Locate and identify every blood parasite.
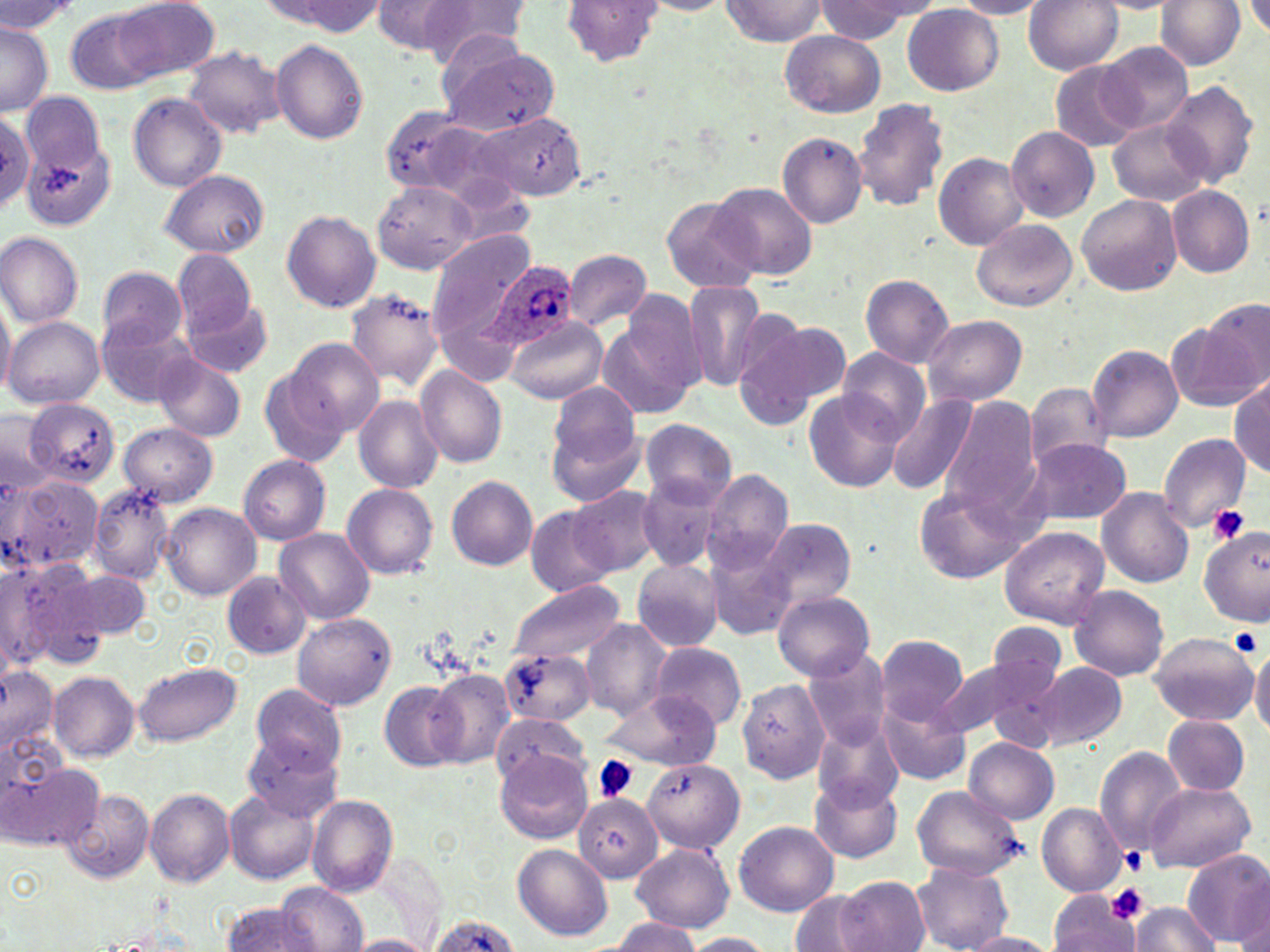

Approximate bounding boxes as (x1, y1, x2, y2) in pixels.
Plasmodium ovale-infected red blood cells: (476, 259, 580, 351).
No Plasmodium falciparum, Plasmodium malariae, Plasmodium vivax, Babesia divergens, or Trypanosoma brucei observed.

Uninfected red blood cell locations: (114, 0, 220, 82), (370, 0, 472, 56), (561, 0, 663, 67), (720, 0, 827, 47), (951, 0, 1052, 18), (1025, 0, 1122, 75), (1156, 0, 1243, 69), (1, 1, 80, 36), (266, 1, 385, 36), (425, 1, 533, 71), (641, 1, 733, 15), (817, 1, 926, 41), (1089, 1, 1179, 14), (1244, 2, 1270, 40), (903, 5, 1003, 95), (65, 6, 163, 93), (0, 24, 52, 114), (780, 31, 885, 117), (269, 39, 369, 144), (1099, 41, 1194, 134), (184, 46, 287, 138), (439, 47, 559, 136), (1048, 60, 1144, 152), (1161, 80, 1261, 186), (21, 91, 106, 175), (128, 93, 227, 192), (852, 98, 951, 212), (377, 107, 483, 196), (1, 110, 37, 213), (469, 112, 588, 200), (1108, 118, 1209, 205), (1006, 125, 1099, 222), (22, 133, 117, 232), (777, 133, 867, 228), (933, 152, 1028, 250), (159, 169, 269, 257), (373, 182, 477, 275), (709, 182, 817, 280), (1167, 185, 1256, 277), (1077, 194, 1182, 297), (661, 196, 762, 294), (281, 211, 380, 311), (973, 219, 1078, 311), (427, 228, 537, 361), (0, 231, 85, 327), (565, 249, 651, 329), (171, 250, 261, 338), (97, 266, 187, 350), (861, 274, 955, 367), (681, 281, 768, 391), (0, 284, 15, 401), (346, 287, 443, 390), (624, 288, 755, 403), (182, 295, 273, 376), (1201, 299, 1269, 393), (599, 306, 702, 420), (96, 311, 196, 407), (730, 311, 842, 426), (4, 314, 106, 410), (923, 315, 1027, 405), (504, 316, 607, 402), (1168, 323, 1260, 413), (284, 340, 384, 439), (1087, 344, 1184, 441), (835, 348, 929, 444), (152, 351, 247, 443), (259, 365, 352, 470), (416, 365, 507, 468), (1230, 375, 1270, 475), (1024, 383, 1114, 467), (547, 384, 642, 485), (804, 392, 904, 492), (888, 393, 981, 497), (355, 395, 442, 494), (938, 396, 1040, 516), (17, 399, 122, 488), (1, 406, 53, 486), (639, 418, 736, 507), (120, 422, 217, 506), (1157, 433, 1251, 531), (1020, 437, 1134, 527), (238, 454, 330, 545), (703, 469, 793, 571), (636, 473, 725, 573), (8, 475, 105, 574), (447, 476, 537, 570), (89, 483, 176, 583), (344, 483, 438, 578), (914, 484, 1030, 582), (568, 487, 665, 576), (1096, 488, 1194, 588), (162, 503, 262, 599), (525, 506, 616, 595), (756, 517, 856, 611), (999, 526, 1109, 628), (1199, 526, 1268, 626), (276, 528, 374, 623), (704, 541, 799, 641), (631, 558, 723, 653), (0, 560, 60, 671), (24, 561, 128, 663), (67, 569, 152, 641), (222, 571, 311, 658), (505, 577, 625, 666), (1068, 584, 1170, 680), (773, 591, 876, 680), (293, 614, 395, 710), (580, 619, 672, 719), (985, 620, 1069, 695), (1148, 632, 1257, 726), (875, 633, 970, 724), (1249, 641, 1270, 739), (649, 642, 747, 727), (804, 648, 892, 752), (502, 649, 595, 725), (944, 655, 1057, 747), (133, 661, 243, 747), (1035, 662, 1127, 750), (0, 664, 59, 751), (428, 670, 514, 767), (49, 672, 139, 762), (736, 678, 828, 784), (378, 680, 464, 770), (248, 683, 347, 777), (600, 689, 720, 770), (878, 694, 973, 785), (493, 713, 592, 790), (1162, 714, 1251, 797), (813, 718, 905, 813), (0, 726, 69, 804), (245, 733, 344, 821), (964, 739, 1059, 824), (1094, 746, 1189, 855), (496, 753, 592, 844), (644, 757, 745, 852), (6, 762, 102, 850), (809, 778, 902, 863), (1143, 780, 1255, 873), (912, 785, 1026, 881), (145, 787, 235, 886), (65, 788, 155, 884), (227, 788, 321, 883), (575, 794, 662, 881), (307, 795, 398, 896), (1037, 803, 1127, 897), (734, 820, 839, 915), (631, 842, 735, 932), (513, 843, 613, 941), (1182, 849, 1270, 947), (911, 862, 1013, 952), (837, 876, 928, 952), (278, 884, 368, 952), (790, 889, 879, 951), (1049, 890, 1141, 952), (1130, 902, 1224, 952), (220, 903, 322, 951), (427, 913, 516, 952), (607, 918, 703, 951), (680, 932, 776, 951), (960, 932, 1059, 951), (348, 934, 436, 952). Platelet locations: (1209, 506, 1247, 543), (1229, 629, 1262, 658), (593, 755, 639, 802), (1118, 847, 1147, 875), (1106, 882, 1150, 925). Slide-level diagnosis: Plasmodium ovale. Image is 1270×952 pixels. Captured at 1000x magnification. One field of a larger specimen. Optical microscopy. May-Grünwald-Giemsa-stained preparation. Thin blood smear.